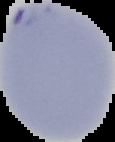

From a thin blood smear. Image is 115×142 pixels. Result: Plasmodium parasites detected. Segmented cell region on a black background.